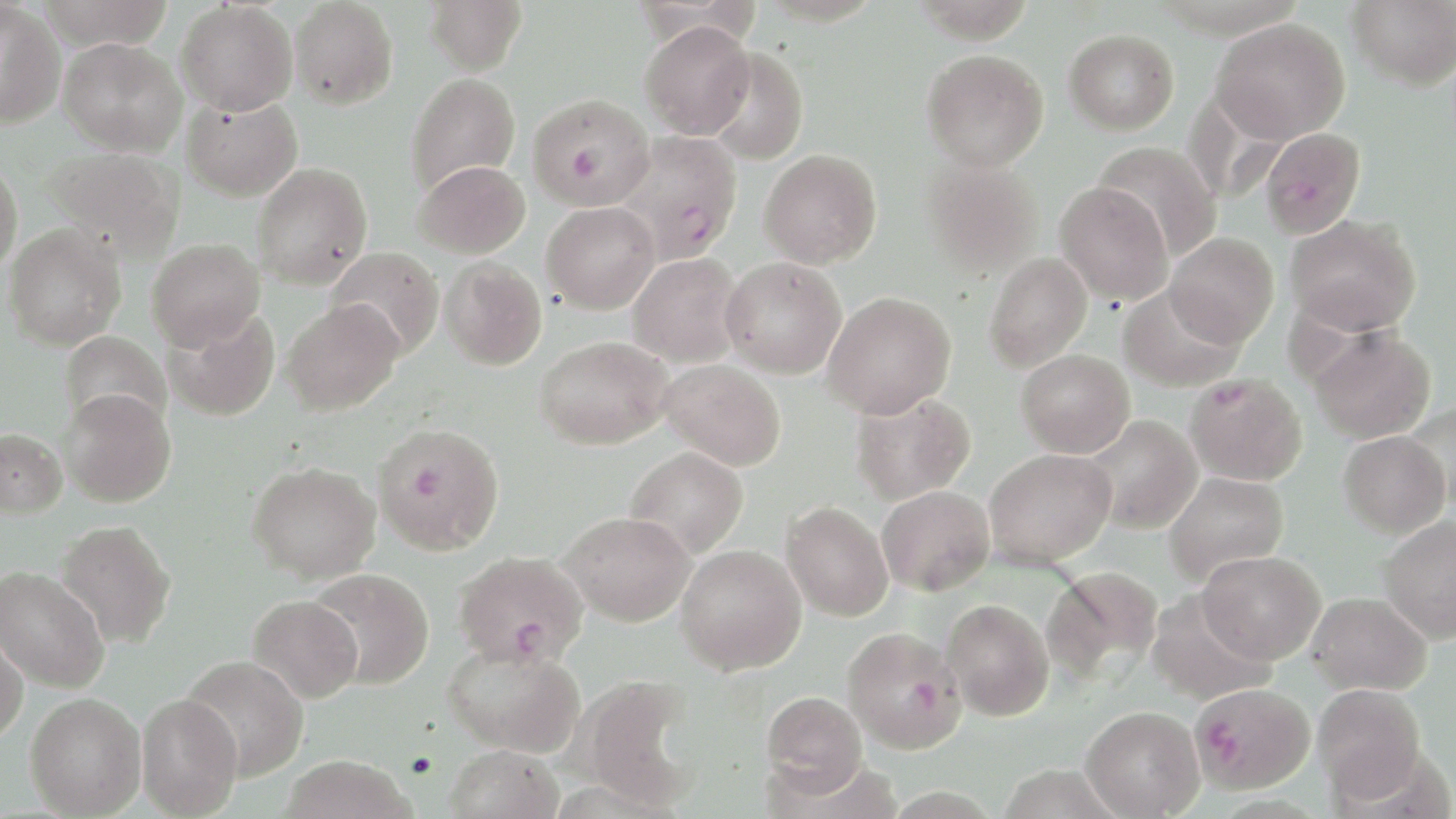

Approximate bounding boxes as (x1,y1)-(x2,y2) corner pairs in pixels. Uninfected red blood cell locations: (37,0)-(175,49), (290,0)-(398,110), (424,0)-(527,75), (1348,0)-(1456,89), (176,2)-(298,115), (0,3)-(67,129), (1210,18)-(1350,143), (639,21)-(755,139), (1064,29)-(1179,135), (58,37)-(186,156), (701,47)-(809,165), (921,49)-(1049,171), (405,73)-(520,196), (182,94)-(303,201), (1092,141)-(1222,261), (43,147)-(184,260), (759,149)-(882,268), (919,155)-(1044,278), (0,158)-(23,274), (412,160)-(530,259), (252,163)-(373,290), (1054,181)-(1174,306), (541,201)-(660,314), (1285,214)-(1421,336), (3,224)-(126,351), (1166,232)-(1279,346), (146,238)-(265,350), (325,246)-(444,360), (983,252)-(1093,373), (626,253)-(746,368), (720,256)-(847,379), (439,257)-(547,370), (1118,284)-(1245,393), (822,291)-(956,419), (281,299)-(403,416), (162,307)-(280,421), (1310,327)-(1436,443), (59,331)-(171,433), (535,335)-(673,449), (1016,349)-(1135,457), (659,360)-(787,471), (59,389)-(176,507), (849,391)-(975,505), (1404,402)-(1456,512), (1084,414)-(1203,533), (0,428)-(68,519), (1339,431)-(1450,538), (625,446)-(748,559), (984,448)-(1116,568), (247,461)-(381,584), (1163,471)-(1288,585), (877,485)-(995,595), (782,501)-(893,621), (558,511)-(696,627), (1379,515)-(1456,643), (54,519)-(176,648), (675,544)-(806,675), (1197,550)-(1325,664), (0,565)-(109,693), (1043,565)-(1164,684), (306,567)-(434,690), (1307,591)-(1432,695), (247,595)-(363,703), (942,598)-(1054,720), (0,629)-(28,744), (442,643)-(585,758), (181,655)-(309,781), (576,675)-(704,810), (1313,683)-(1426,800), (761,691)-(867,795), (24,692)-(146,818), (136,693)-(243,818), (1080,706)-(1204,818), (444,744)-(563,819), (281,755)-(415,819). Plasmodium falciparum-infected red blood cell locations: (527,92)-(655,211), (1260,127)-(1365,239), (613,131)-(744,263), (1185,372)-(1307,486), (373,422)-(504,555), (453,550)-(588,667), (842,626)-(966,753), (1191,684)-(1312,792). Slide-level diagnosis: Plasmodium falciparum. Captured at 1000x magnification. Single field of view. May-Grünwald-Giemsa-stained preparation. Thin blood film. Image is 1456×819 pixels. Light microscopy.